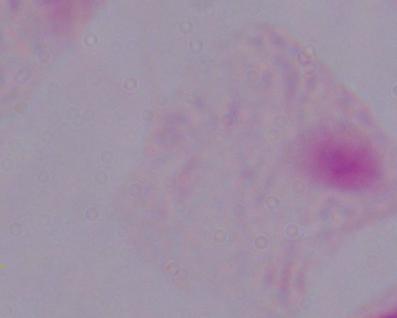 A trichomonad is shown. Micrograph. Captured at 1000x magnification.